Identify the cell.
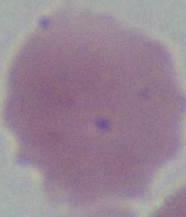
An erythrocyte.

{
  "modality": "photomicrograph",
  "magnification": "1000x"
}